Outline each uninfected red blood cell.
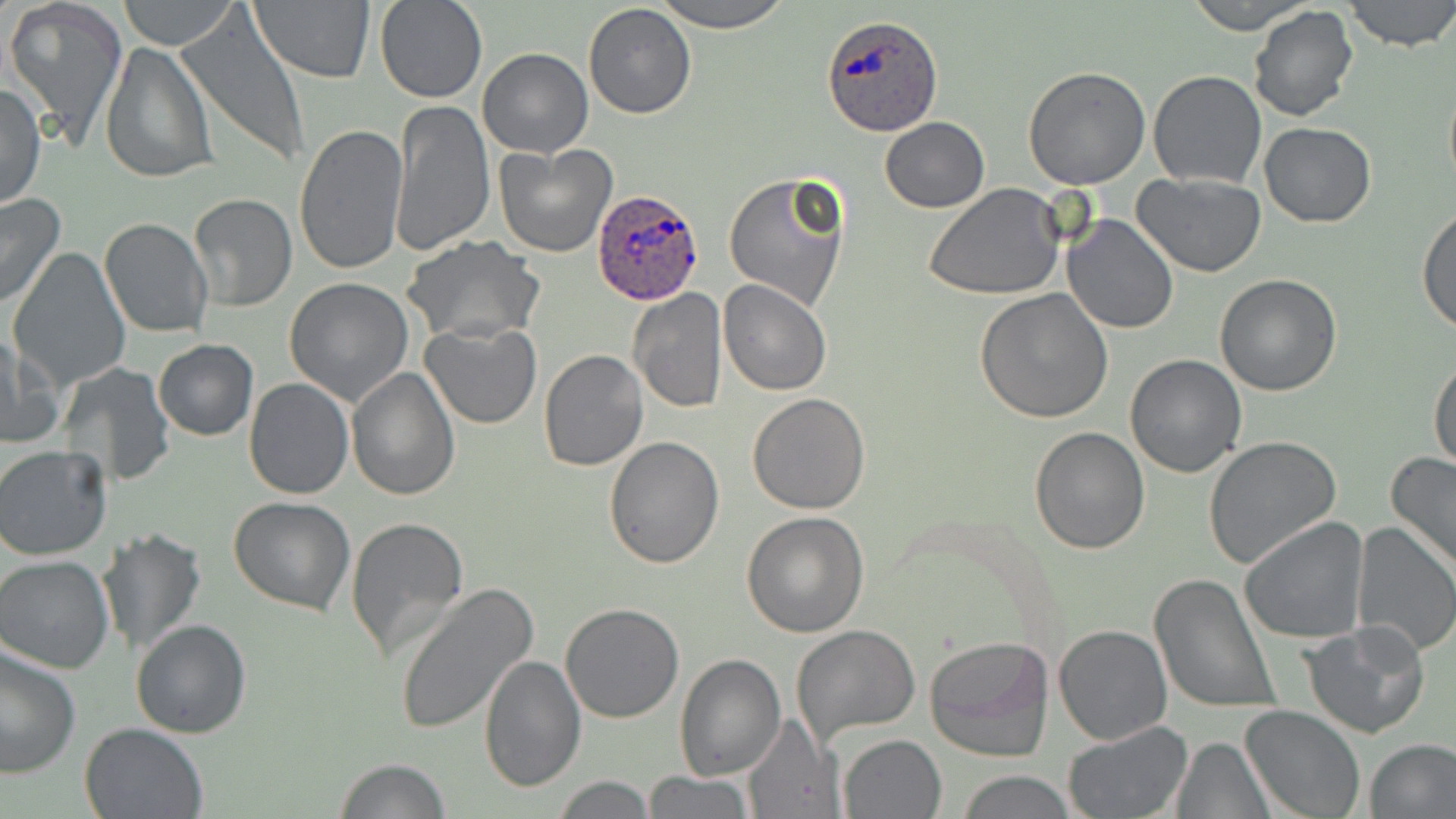

Approximate bounding boxes as [x1, y1, x2, y2] in pixels.
Uninfected red blood cells (subset): [118, 0, 240, 50], [248, 0, 375, 86], [375, 0, 487, 103], [651, 0, 796, 31], [1183, 0, 1319, 34], [1342, 0, 1456, 52], [4, 1, 128, 149], [583, 2, 697, 120], [1248, 5, 1359, 123], [177, 13, 310, 168], [100, 41, 216, 185], [478, 48, 593, 159], [1022, 66, 1151, 190], [1148, 70, 1267, 190], [1443, 77, 1456, 196], [1, 81, 46, 211], [390, 99, 495, 257], [879, 117, 989, 212], [295, 121, 409, 277], [1259, 122, 1376, 227], [723, 171, 851, 310], [1131, 172, 1266, 277], [922, 184, 1066, 298], [187, 192, 297, 312], [0, 193, 66, 309], [1418, 206, 1456, 334], [1063, 214, 1179, 334], [98, 217, 213, 338], [402, 237, 545, 346], [7, 247, 133, 392], [1214, 273, 1342, 395], [285, 277, 416, 406], [717, 280, 832, 396], [628, 288, 727, 412], [974, 289, 1114, 426], [420, 322, 543, 431], [3, 330, 51, 451], [153, 339, 257, 442], [538, 350, 648, 472], [1429, 352, 1455, 473], [1125, 354, 1249, 477], [58, 361, 175, 486], [348, 365, 461, 501], [243, 378, 352, 498], [747, 393, 871, 515], [1029, 425, 1148, 554], [1203, 435, 1342, 570], [604, 437, 725, 570], [0, 444, 113, 561], [1386, 451, 1456, 577], [230, 496, 356, 616], [741, 511, 869, 637], [1240, 515, 1369, 645], [344, 516, 470, 662], [1350, 519, 1456, 656], [96, 528, 207, 656], [0, 556, 118, 674], [1150, 574, 1281, 716], [393, 585, 539, 735], [560, 603, 684, 723], [131, 618, 252, 737], [1302, 621, 1431, 740], [792, 624, 920, 743], [1052, 624, 1171, 745], [924, 635, 1054, 762], [0, 646, 81, 779], [674, 653, 787, 779], [478, 655, 587, 793], [1239, 703, 1366, 818], [741, 715, 843, 819], [78, 721, 208, 819], [1060, 721, 1190, 819], [838, 733, 946, 817], [1173, 737, 1273, 818], [1365, 738, 1456, 817], [334, 758, 453, 818], [958, 769, 1075, 819], [643, 771, 754, 819], [549, 775, 657, 816].

slide-level diagnosis = Plasmodium ovale
image size = 1456×819 pixels
modality = light microscopy
stain = May-Grünwald-Giemsa
Plasmodium ovale-infected red blood cell locations (subset) = approximate bounding boxes as [x1, y1, x2, y2] in pixels: [822, 14, 942, 136], [594, 188, 706, 303]
field of view = one of a larger specimen
magnification = 1000x
preparation = thin blood film